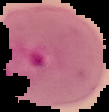

image type = segmented cell region on a black background
malaria status = parasitized
image size = 109×112 pixels
preparation = thin blood film